Give the position of every leukocyte visible.
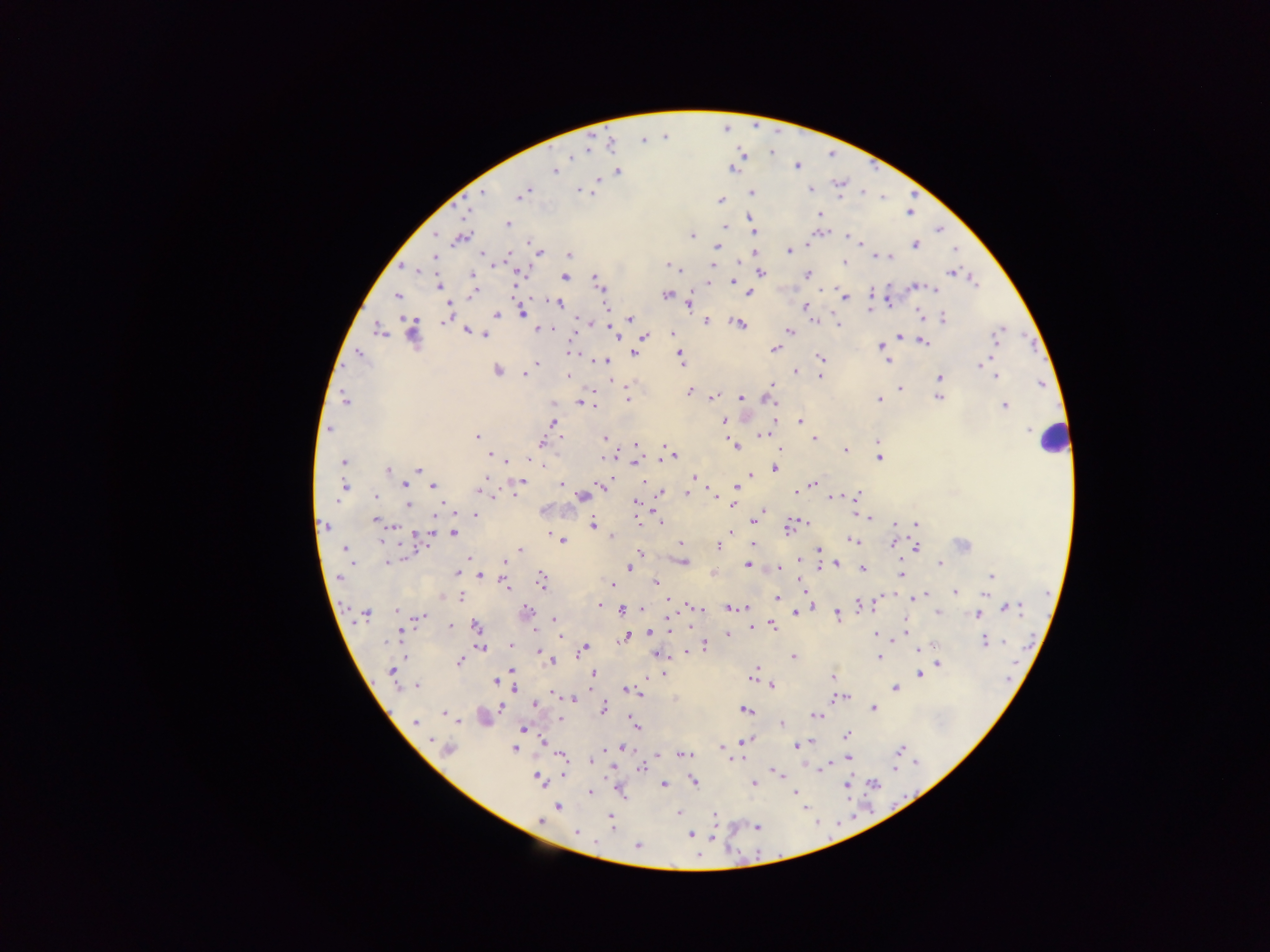
Approximate centers as {x, y} in pixels.
Leukocytes: {1050, 440}.

Malaria parasite locations: {796, 165}, {733, 169}, {554, 171}, {618, 171}, {598, 179}, {810, 189}, {527, 190}, {580, 190}, {483, 192}, {751, 192}, {522, 193}, {586, 193}, {720, 200}, {820, 213}, {751, 218}, {508, 224}, {725, 227}, {436, 234}, {755, 234}, {691, 236}, {848, 237}, {461, 238}, {859, 242}, {807, 243}, {915, 245}, {716, 247}, {788, 251}, {540, 252}, {482, 255}, {569, 255}, {435, 256}, {877, 256}, {891, 257}, {844, 262}, {670, 265}, {713, 265}, {674, 268}, {417, 270}, {761, 272}, {950, 273}, {519, 274}, {807, 274}, {472, 275}, {564, 277}, {974, 281}, {734, 282}, {708, 283}, {599, 284}, {438, 286}, {915, 286}, {824, 288}, {935, 290}, {473, 293}, {749, 293}, {398, 295}, {666, 295}, {845, 299}, {887, 299}, {558, 303}, {690, 304}, {606, 306}, {805, 306}, {869, 311}, {522, 313}, {496, 314}, {918, 314}, {630, 318}, {943, 319}, {445, 320}, {582, 320}, {705, 321}, {815, 321}, {836, 321}, {738, 324}, {838, 325}, {539, 328}, {379, 331}, {412, 332}, {467, 332}, {789, 332}, {614, 333}, {672, 334}, {997, 334}, {486, 335}, {645, 336}, {899, 336}, {923, 342}, {880, 346}, {775, 349}, {570, 352}, {359, 353}, {635, 353}, {679, 353}, {821, 358}, {887, 360}, {605, 361}, {537, 362}, {683, 362}, {980, 365}, {497, 370}, {795, 371}, {525, 375}, {568, 375}, {820, 376}, {996, 376}, {940, 377}, {617, 381}, {772, 384}, {900, 389}, {939, 390}, {690, 392}, {939, 397}, {712, 398}, {740, 398}, {770, 398}, {628, 399}, {879, 399}, {345, 400}, {581, 402}, {1004, 406}, {553, 421}, {724, 421}, {800, 421}, {330, 429}, {768, 432}, {762, 434}, {477, 437}, {605, 437}, {560, 438}, {813, 438}, {877, 442}, {541, 443}, {636, 444}, {735, 446}, {663, 447}, {780, 449}, {845, 450}, {490, 455}, {671, 456}, {662, 458}, {879, 458}, {602, 459}, {507, 461}, {344, 462}, {634, 463}, {542, 464}, {418, 468}, {775, 468}, {388, 470}, {750, 474}, {693, 477}, {485, 478}, {645, 481}, {521, 482}, {404, 484}, {561, 484}, {601, 484}, {813, 484}, {345, 486}, {433, 486}, {736, 487}, {689, 489}, {796, 492}, {488, 493}, {515, 493}, {688, 493}, {660, 494}, {716, 494}, {856, 495}, {376, 496}, {581, 496}, {831, 497}, {336, 501}, {636, 503}, {408, 504}, {765, 511}, {760, 513}, {855, 514}, {475, 515}, {868, 518}, {660, 519}, {375, 520}, {638, 522}, {895, 524}, {916, 524}, {593, 525}, {393, 526}, {325, 527}, {788, 528}, {730, 532}, {453, 533}, {420, 535}, {612, 536}, {852, 539}, {382, 540}, {562, 541}, {680, 543}, {893, 543}, {962, 544}, {717, 546}, {752, 546}, {917, 548}, {344, 549}, {519, 549}, {819, 550}, {639, 552}, {469, 558}, {799, 559}, {504, 561}, {684, 561}, {387, 562}, {351, 564}, {836, 564}, {940, 564}, {748, 565}, {821, 566}, {630, 568}, {780, 568}, {862, 568}, {456, 572}, {902, 573}, {480, 575}, {991, 576}, {339, 578}, {541, 580}, {612, 584}, {656, 584}, {506, 585}, {955, 591}, {921, 595}, {985, 595}, {462, 597}, {777, 598}, {914, 598}, {667, 601}, {600, 605}, {861, 605}, {694, 606}, {811, 606}, {1009, 607}, {697, 608}, {746, 608}, {623, 609}, {641, 609}, {730, 609}, {396, 611}, {526, 611}, {938, 613}, {365, 614}, {796, 614}, {977, 614}, {668, 615}, {837, 616}, {419, 617}, {553, 621}, {450, 626}, {773, 626}, {476, 627}, {751, 627}, {905, 630}, {400, 632}, {649, 632}, {876, 634}, {559, 636}, {727, 636}, {626, 637}, {894, 639}, {985, 642}, {510, 644}, {705, 645}, {480, 648}, {585, 648}, {920, 648}, {686, 652}, {540, 653}, {656, 654}, {793, 656}, {879, 656}, {551, 662}, {460, 663}, {938, 664}, {512, 669}, {756, 670}, {392, 671}, {593, 674}, {664, 674}, {920, 674}, {833, 676}, {752, 678}, {495, 681}, {772, 685}, {417, 686}, {894, 687}, {514, 689}, {625, 689}, {638, 693}, {553, 694}, {844, 697}, {839, 698}, {573, 700}, {534, 705}, {501, 707}, {604, 708}, {873, 708}, {745, 710}, {443, 714}, {816, 715}, {559, 719}, {458, 722}, {415, 723}, {781, 724}, {636, 726}, {523, 729}, {847, 735}, {431, 740}, {542, 741}, {745, 741}, {797, 746}, {722, 747}, {515, 748}, {622, 748}, {449, 749}, {901, 750}, {683, 755}, {561, 757}, {736, 759}, {848, 759}, {591, 761}, {826, 766}, {894, 767}, {641, 768}, {565, 773}, {777, 775}, {538, 778}, {695, 781}, {754, 783}, {874, 784}, {664, 785}, {847, 785}, {590, 792}, {796, 793}, {558, 806}, {678, 813}, {715, 815}, {610, 817}, {541, 820}, {611, 824}, {757, 827}, {576, 832}, {690, 835}, {637, 846}. Sample from Ghana. One field of view. Image is 1270×952 pixels. Thick blood film. Mobile-phone photograph taken through the microscope.